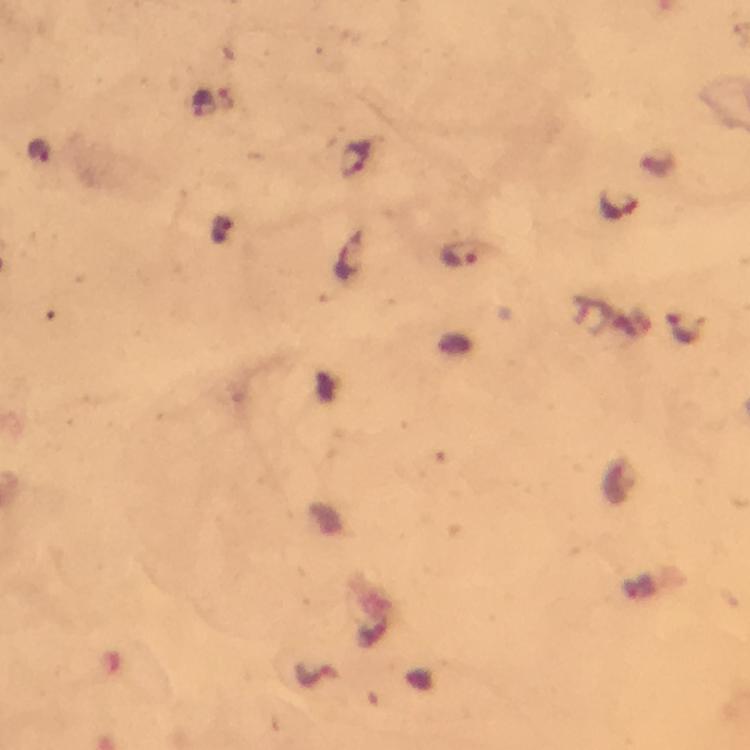
{
  "preparation": "thick blood smear",
  "image_size": "750×750 pixels",
  "cropped_from": "a single field of view",
  "immersion_oil": "used",
  "stain": "Giemsa",
  "context": "from a malaria diagnostic workup",
  "plasmodium_parasite_locations": "approximate centers as {x, y} in pixels: {356, 161}, {615, 206}, {461, 254}, {684, 328}",
  "magnification": "100x",
  "capture": "smartphone photograph through a microscope"
}